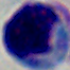

identification = white blood cell
magnification = 1000x
modality = micrograph